State which cell type is depicted.
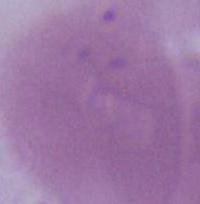
This is an erythrocyte.

Summary:
  - Modality: photomicrograph
  - Magnification: 1000x